Classify this cell by malaria status.
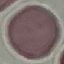

It is uninfected.

Giemsa-stained preparation. Automatically extracted cell patch, resized to 64 × 64 pixels. Acquired by smartphone through the microscope eyepiece. Thin blood smear.